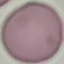
Summary:
  - Result: no malaria parasites seen
  - Stain: Giemsa
  - Capture: smartphone through the microscope eyepiece
  - Preparation: thin blood smear
  - Image type: automatically extracted cell patch, resized to 64 × 64 pixels